Report the malaria status of this cell.
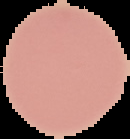

Uninfected.

Summary:
  - Preparation: thin blood smear
  - Image type: cell region segmented out of the field of view; surrounding area masked to black
  - Image size: 130×139 pixels